State which parasite is depicted.
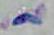
Toxoplasma gondii.

Summary:
  - Magnification: 1000x
  - Modality: photomicrograph